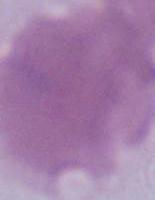
Captured at 1000x magnification. Photomicrograph. An erythrocyte is seen.